Classify this cell by malaria status.
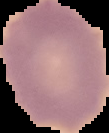

It is uninfected.

image type = segmented cell region with the area outside set to black
preparation = thin blood film
image size = 109×133 pixels